Comment on the morphology of the erythrocytes.
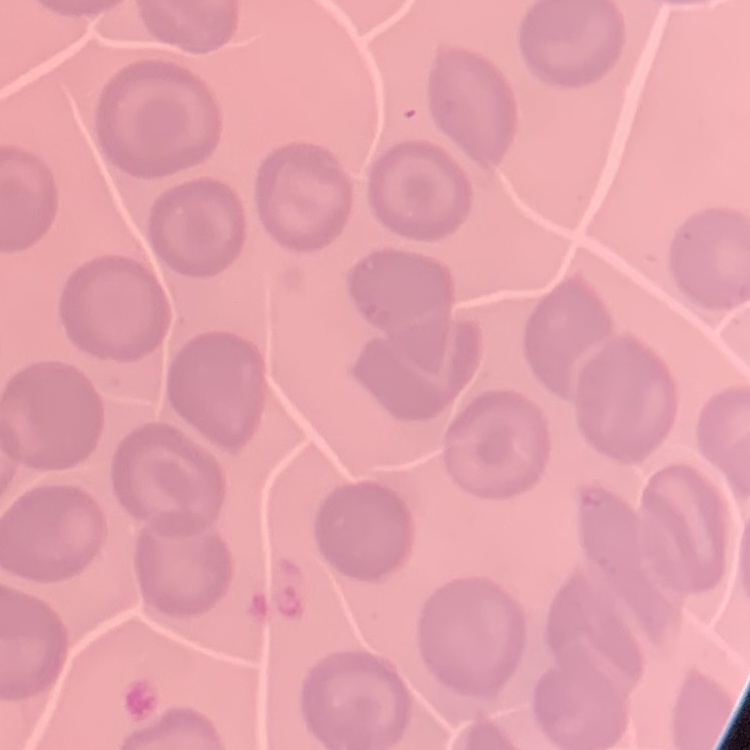
They show no rouleaux formation.

Summary:
  - Preparation: thin peripheral smear
  - Image type: one tile cut from a larger photomicrograph
  - Stain: Field's or Giemsa